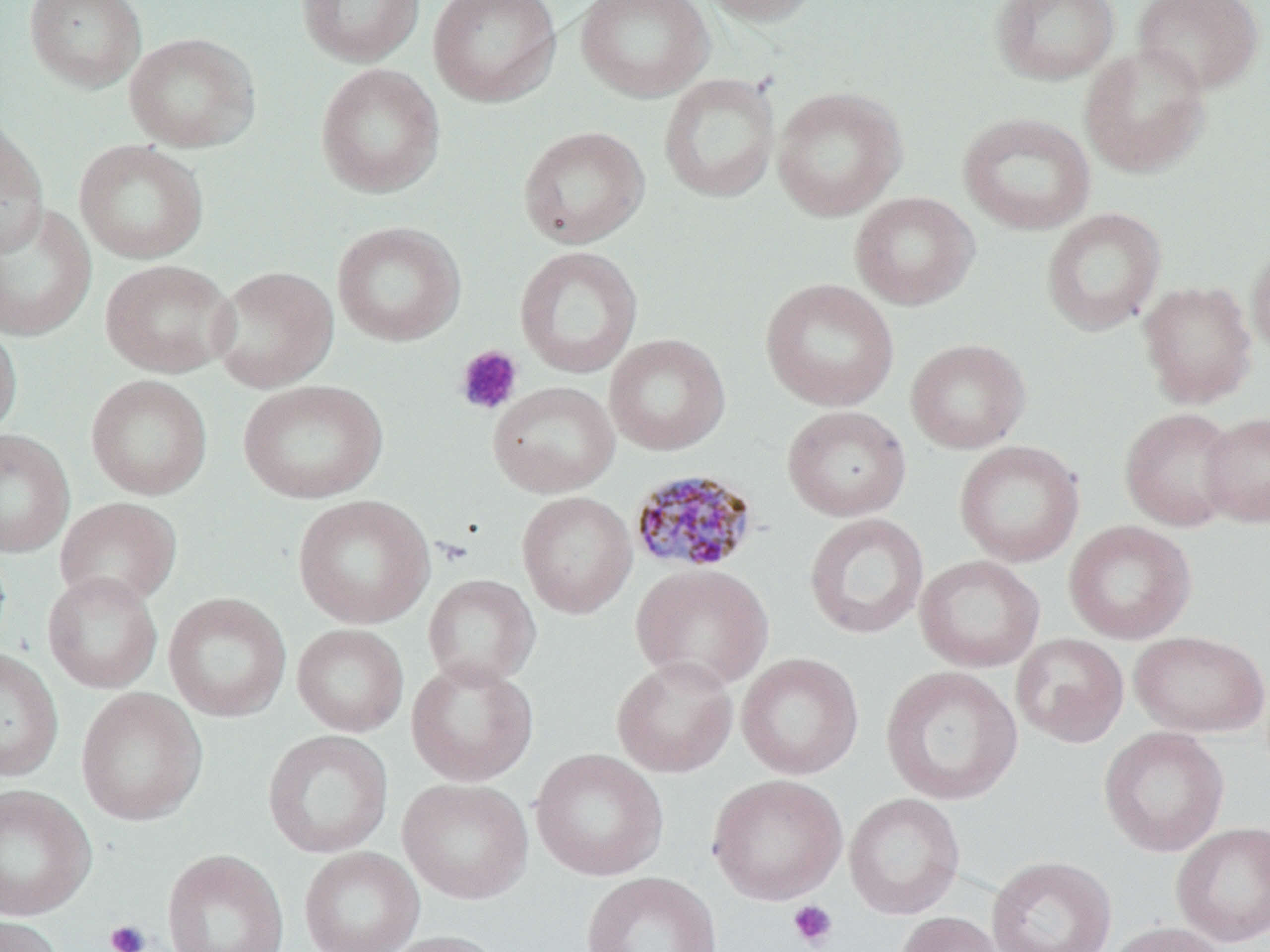
Summary:
  - Coordinate format: approximate bounding boxes as [x1, y1, x2, y2] in pixels
  - Uninfected red blood cell locations: [24, 0, 146, 93], [296, 0, 425, 67], [428, 0, 561, 107], [574, 0, 713, 102], [696, 0, 825, 26], [990, 0, 1121, 85], [1133, 0, 1264, 95], [124, 32, 261, 153], [1079, 42, 1211, 178], [315, 63, 445, 198], [658, 72, 780, 204], [771, 86, 907, 222], [957, 112, 1096, 236], [0, 120, 49, 259], [517, 125, 649, 249], [74, 139, 208, 264], [850, 192, 980, 310], [0, 204, 97, 342], [1041, 208, 1166, 336], [332, 221, 466, 346], [1246, 240, 1270, 359], [513, 245, 643, 380], [99, 259, 238, 378], [209, 265, 339, 393], [759, 277, 899, 412], [1138, 280, 1257, 408], [0, 319, 22, 440], [604, 333, 731, 456], [905, 338, 1030, 454], [86, 374, 213, 500], [238, 379, 388, 504], [488, 381, 620, 497], [781, 405, 912, 522], [1119, 407, 1240, 531], [1199, 411, 1270, 528], [0, 428, 75, 558], [954, 440, 1084, 568], [516, 490, 637, 619], [292, 494, 435, 629], [55, 496, 183, 609], [804, 512, 929, 640], [1063, 520, 1196, 644], [914, 555, 1045, 673], [630, 563, 774, 691], [42, 571, 163, 694], [422, 574, 541, 688], [163, 592, 291, 722], [292, 623, 409, 737], [1128, 630, 1269, 738], [1011, 633, 1129, 747], [0, 647, 63, 782], [736, 652, 864, 779], [611, 655, 738, 778], [406, 657, 539, 786], [881, 665, 1023, 806], [75, 687, 208, 826], [1098, 726, 1229, 857], [262, 729, 394, 859], [530, 748, 668, 881], [708, 773, 848, 905], [398, 778, 533, 905], [0, 784, 96, 921], [843, 793, 965, 919], [1171, 821, 1270, 946], [299, 846, 425, 952], [162, 849, 289, 952], [986, 855, 1116, 952], [581, 871, 722, 952], [895, 911, 1006, 952], [0, 915, 65, 952], [1105, 921, 1232, 952], [376, 930, 506, 952]
  - Platelet locations: [455, 345, 523, 415], [788, 900, 838, 950], [104, 919, 151, 952]
  - Plasmodium malariae-infected red blood cell locations: [628, 468, 761, 575]
  - Slide-level diagnosis: Plasmodium malariae
  - Stain: May-Grünwald-Giemsa
  - Preparation: thin blood film
  - Modality: light microscopy
  - Magnification: 1000x
  - Field of view: one of a larger specimen
  - Image size: 1270×952 pixels